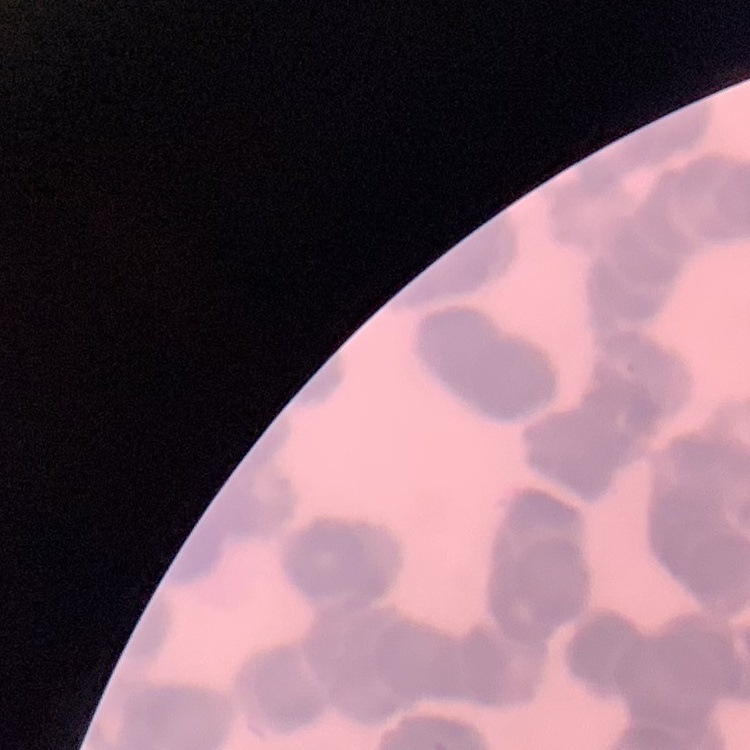

The erythrocytes show rouleaux formation. Square crop of a larger photomicrograph. Thin blood smear. Stained with either Field's or Giemsa.